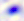

magnification = 400x
identification = Toxoplasma gondii
modality = micrograph